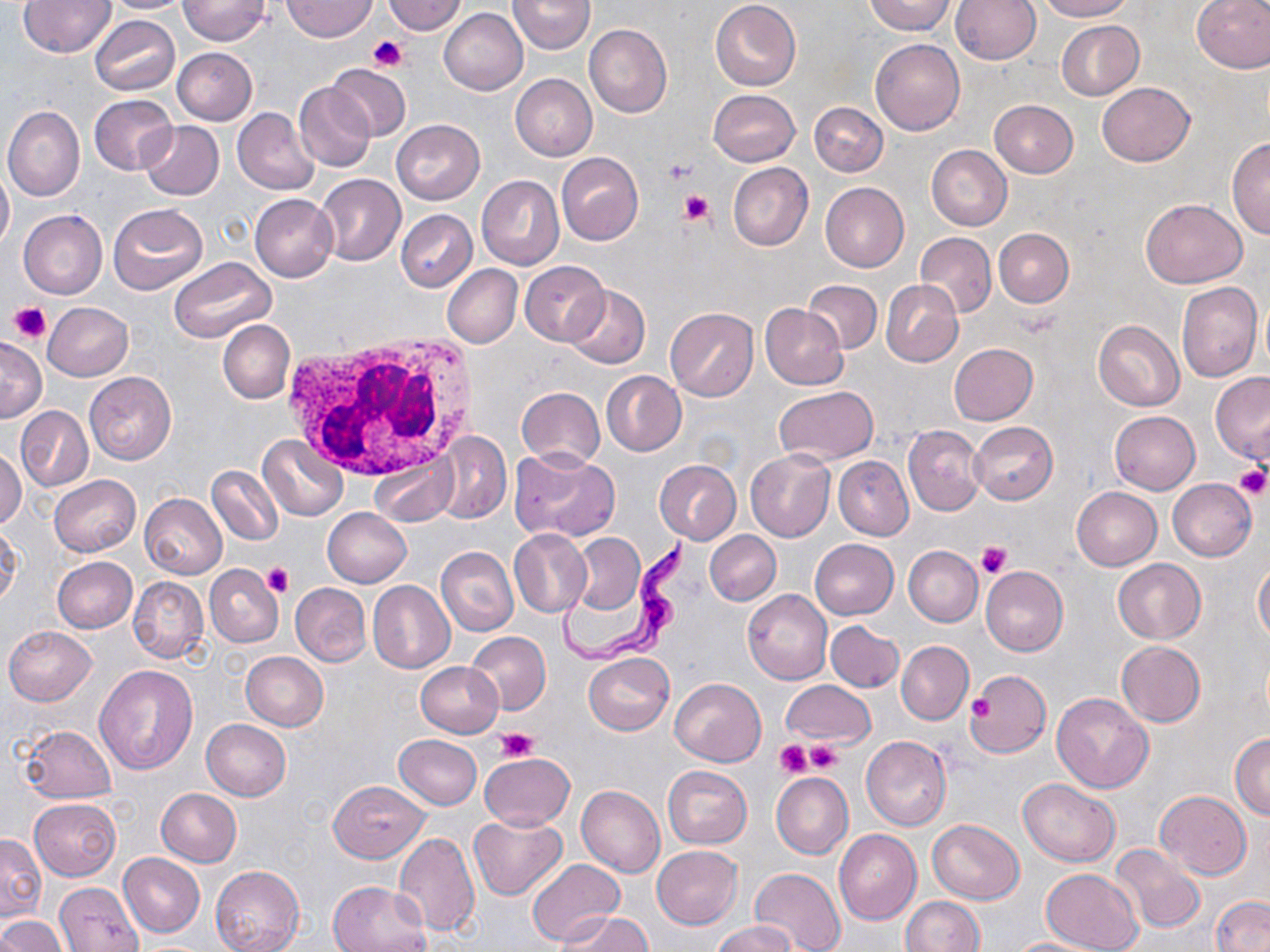

Approximate bounding boxes as named x1/y1/x2/y2 corners in pixels. Platelet locations: (x1=368, y1=35, x2=408, y2=71), (x1=660, y1=158, x2=697, y2=189), (x1=679, y1=189, x2=713, y2=224), (x1=9, y1=302, x2=53, y2=344), (x1=1233, y1=464, x2=1269, y2=500), (x1=977, y1=541, x2=1014, y2=579), (x1=264, y1=563, x2=294, y2=598), (x1=964, y1=683, x2=1002, y2=736), (x1=967, y1=695, x2=994, y2=720), (x1=498, y1=728, x2=537, y2=763), (x1=773, y1=739, x2=812, y2=778), (x1=805, y1=741, x2=842, y2=775). White blood cell locations: (x1=283, y1=327, x2=483, y2=485). Trypanosoma brucei locations: (x1=554, y1=533, x2=692, y2=668). Uninfected red blood cell locations: (x1=19, y1=0, x2=115, y2=57), (x1=100, y1=0, x2=196, y2=13), (x1=178, y1=0, x2=269, y2=45), (x1=281, y1=0, x2=377, y2=42), (x1=508, y1=0, x2=595, y2=54), (x1=710, y1=0, x2=801, y2=91), (x1=862, y1=0, x2=955, y2=34), (x1=951, y1=0, x2=1040, y2=65), (x1=1037, y1=0, x2=1132, y2=21), (x1=1192, y1=0, x2=1270, y2=73), (x1=383, y1=1, x2=469, y2=34), (x1=439, y1=8, x2=528, y2=95), (x1=90, y1=15, x2=180, y2=96), (x1=1056, y1=20, x2=1143, y2=100), (x1=584, y1=24, x2=673, y2=118), (x1=870, y1=39, x2=964, y2=136), (x1=172, y1=47, x2=258, y2=125), (x1=328, y1=65, x2=411, y2=141), (x1=510, y1=74, x2=597, y2=160), (x1=1097, y1=82, x2=1195, y2=165), (x1=294, y1=83, x2=376, y2=171), (x1=708, y1=89, x2=800, y2=166), (x1=88, y1=93, x2=177, y2=175), (x1=990, y1=100, x2=1079, y2=178), (x1=810, y1=102, x2=887, y2=177), (x1=2, y1=106, x2=84, y2=201), (x1=232, y1=109, x2=319, y2=194), (x1=391, y1=120, x2=485, y2=204), (x1=139, y1=121, x2=224, y2=200), (x1=1227, y1=136, x2=1270, y2=239), (x1=927, y1=145, x2=1011, y2=230), (x1=556, y1=152, x2=644, y2=244), (x1=728, y1=162, x2=813, y2=251), (x1=0, y1=164, x2=13, y2=251), (x1=314, y1=173, x2=406, y2=265), (x1=476, y1=175, x2=563, y2=270), (x1=820, y1=182, x2=909, y2=272), (x1=249, y1=194, x2=337, y2=282), (x1=1140, y1=198, x2=1249, y2=289), (x1=107, y1=204, x2=208, y2=296), (x1=396, y1=209, x2=477, y2=292), (x1=19, y1=211, x2=107, y2=298), (x1=994, y1=228, x2=1073, y2=307), (x1=916, y1=233, x2=997, y2=317), (x1=169, y1=257, x2=276, y2=343), (x1=520, y1=261, x2=610, y2=346), (x1=442, y1=265, x2=522, y2=348), (x1=881, y1=280, x2=962, y2=367), (x1=803, y1=281, x2=882, y2=353), (x1=1176, y1=281, x2=1261, y2=383), (x1=564, y1=285, x2=650, y2=369), (x1=43, y1=302, x2=133, y2=381), (x1=760, y1=303, x2=847, y2=389), (x1=664, y1=307, x2=759, y2=400), (x1=218, y1=320, x2=294, y2=403), (x1=1093, y1=320, x2=1185, y2=411), (x1=0, y1=337, x2=45, y2=422), (x1=948, y1=343, x2=1038, y2=425), (x1=85, y1=371, x2=176, y2=465), (x1=601, y1=371, x2=686, y2=456), (x1=1210, y1=371, x2=1270, y2=464), (x1=516, y1=386, x2=604, y2=469), (x1=775, y1=386, x2=877, y2=464), (x1=15, y1=407, x2=92, y2=493), (x1=1109, y1=411, x2=1200, y2=494), (x1=968, y1=421, x2=1057, y2=504), (x1=902, y1=425, x2=985, y2=516), (x1=433, y1=433, x2=512, y2=523), (x1=257, y1=434, x2=348, y2=520), (x1=1, y1=447, x2=25, y2=528), (x1=510, y1=448, x2=619, y2=542), (x1=746, y1=451, x2=835, y2=542), (x1=369, y1=452, x2=458, y2=529), (x1=833, y1=456, x2=913, y2=540), (x1=654, y1=460, x2=742, y2=544), (x1=207, y1=464, x2=282, y2=545), (x1=49, y1=475, x2=140, y2=556), (x1=1167, y1=479, x2=1256, y2=561), (x1=1070, y1=487, x2=1162, y2=570), (x1=139, y1=493, x2=227, y2=579), (x1=323, y1=507, x2=412, y2=587), (x1=0, y1=521, x2=22, y2=608), (x1=508, y1=529, x2=592, y2=618), (x1=705, y1=530, x2=780, y2=604), (x1=570, y1=533, x2=646, y2=616), (x1=809, y1=539, x2=898, y2=620), (x1=436, y1=545, x2=518, y2=637), (x1=903, y1=545, x2=983, y2=626), (x1=52, y1=557, x2=137, y2=633), (x1=1113, y1=559, x2=1205, y2=643), (x1=1254, y1=562, x2=1270, y2=646), (x1=205, y1=565, x2=282, y2=648), (x1=980, y1=565, x2=1068, y2=656), (x1=128, y1=577, x2=209, y2=663), (x1=367, y1=581, x2=455, y2=674), (x1=289, y1=582, x2=370, y2=666), (x1=743, y1=590, x2=833, y2=685), (x1=826, y1=621, x2=903, y2=692), (x1=4, y1=625, x2=96, y2=705), (x1=467, y1=631, x2=551, y2=714), (x1=896, y1=640, x2=973, y2=725), (x1=1116, y1=641, x2=1205, y2=727), (x1=241, y1=652, x2=328, y2=731), (x1=584, y1=653, x2=674, y2=735), (x1=416, y1=660, x2=504, y2=737), (x1=94, y1=664, x2=199, y2=775), (x1=967, y1=671, x2=1049, y2=758), (x1=670, y1=678, x2=766, y2=765), (x1=781, y1=681, x2=875, y2=747), (x1=1051, y1=692, x2=1154, y2=792), (x1=201, y1=719, x2=290, y2=801), (x1=20, y1=724, x2=117, y2=803), (x1=1230, y1=733, x2=1270, y2=819), (x1=394, y1=735, x2=482, y2=809), (x1=862, y1=735, x2=952, y2=830), (x1=480, y1=753, x2=574, y2=829), (x1=663, y1=765, x2=752, y2=848), (x1=772, y1=772, x2=853, y2=859), (x1=1018, y1=779, x2=1119, y2=865), (x1=328, y1=780, x2=429, y2=863), (x1=576, y1=784, x2=666, y2=876), (x1=156, y1=788, x2=242, y2=867), (x1=1155, y1=790, x2=1251, y2=880), (x1=29, y1=798, x2=121, y2=881), (x1=468, y1=814, x2=567, y2=900), (x1=927, y1=819, x2=1024, y2=904), (x1=834, y1=829, x2=921, y2=925), (x1=392, y1=831, x2=480, y2=936), (x1=0, y1=834, x2=45, y2=922), (x1=1108, y1=844, x2=1206, y2=933), (x1=652, y1=845, x2=742, y2=929), (x1=118, y1=853, x2=205, y2=937), (x1=527, y1=859, x2=624, y2=945), (x1=210, y1=865, x2=304, y2=951), (x1=749, y1=867, x2=845, y2=952), (x1=1040, y1=868, x2=1143, y2=952), (x1=327, y1=880, x2=432, y2=952), (x1=56, y1=882, x2=143, y2=951), (x1=1211, y1=896, x2=1270, y2=952), (x1=900, y1=897, x2=985, y2=952), (x1=560, y1=913, x2=652, y2=952), (x1=0, y1=915, x2=66, y2=952), (x1=711, y1=920, x2=799, y2=952), (x1=1002, y1=937, x2=1108, y2=951). Slide-level diagnosis: Trypanosoma brucei. May-Grünwald-Giemsa stain. One field of a larger specimen. Thin blood smear. Optical microscopy. Image is 1270×952 pixels. Captured at 1000x magnification.